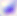
Toxoplasma gondii is shown. 400x magnification. Photomicrograph.